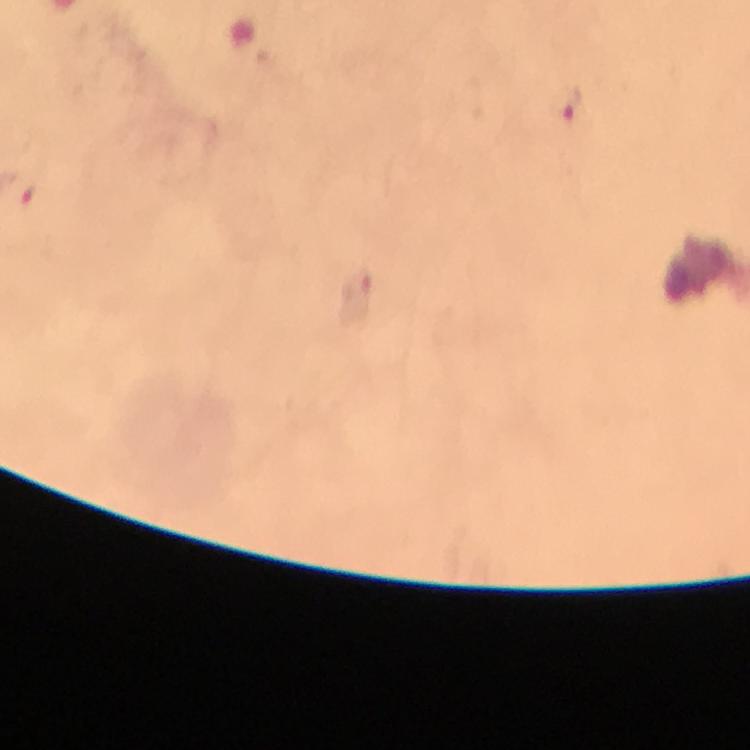

image size = 750×750 pixels
Plasmodium parasite locations = approximate centers as (x, y) in pixels: (568, 107), (358, 284)
cropped from = a single field of view
immersion oil = used
context = from a malaria diagnostic workup
capture = smartphone camera through the microscope
stain = Giemsa
magnification = 100x
preparation = thick blood film